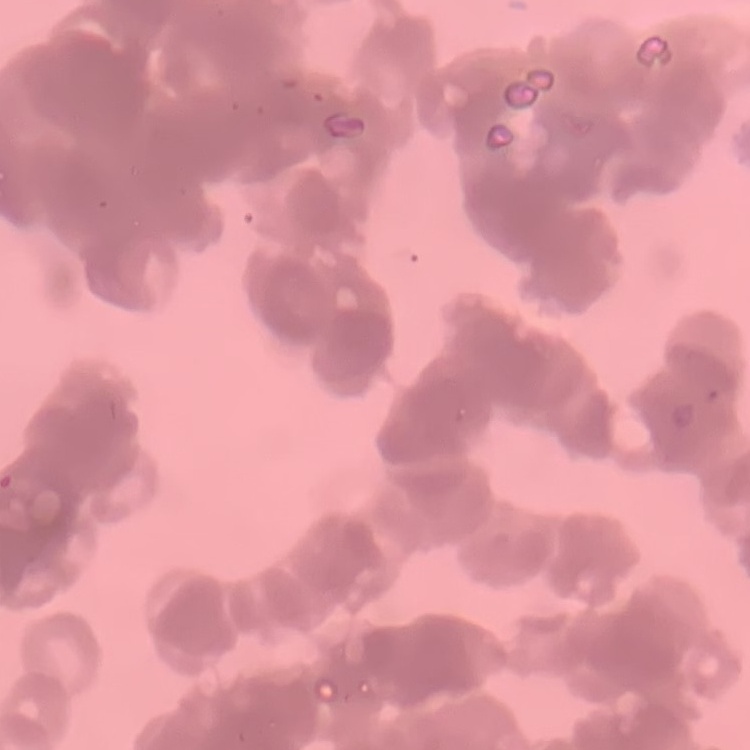
{
  "red_blood_cell_morphology": "rouleaux formation",
  "stain": "Field's or Giemsa",
  "image_type": "square crop of a larger photomicrograph",
  "preparation": "thin blood film"
}